Classify this cell by malaria status.
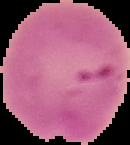

It is parasitized.

Summary:
  - Image type: cell region segmented out of the field of view; surrounding area masked to black
  - Image size: 130×145 pixels
  - Preparation: thin blood smear